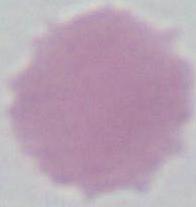

modality = photomicrograph
identification = red blood cell
magnification = 1000x